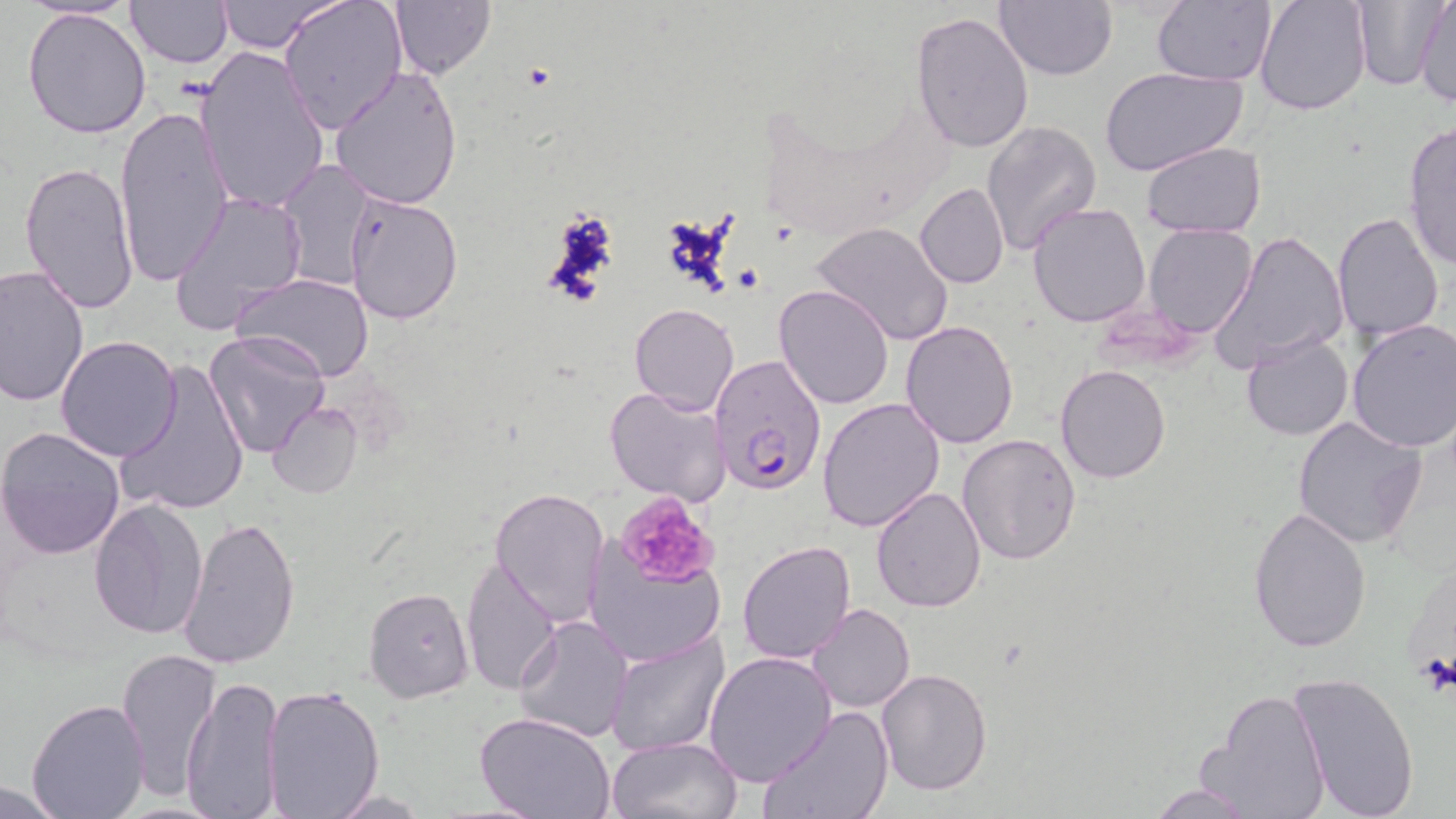
Approximate bounding boxes as named x1/y1/x2/y2 corners in pixels. Uninfected red blood cell locations: (x1=211, y1=0, x2=340, y2=53), (x1=278, y1=0, x2=405, y2=136), (x1=995, y1=0, x2=1116, y2=81), (x1=1151, y1=0, x2=1276, y2=86), (x1=1255, y1=0, x2=1372, y2=116), (x1=1352, y1=0, x2=1443, y2=90), (x1=1414, y1=0, x2=1456, y2=107), (x1=25, y1=1, x2=140, y2=22), (x1=124, y1=1, x2=232, y2=68), (x1=388, y1=1, x2=494, y2=79), (x1=23, y1=7, x2=151, y2=140), (x1=911, y1=12, x2=1036, y2=155), (x1=192, y1=46, x2=331, y2=215), (x1=329, y1=64, x2=464, y2=210), (x1=1099, y1=66, x2=1250, y2=177), (x1=115, y1=104, x2=235, y2=291), (x1=981, y1=120, x2=1102, y2=257), (x1=1401, y1=121, x2=1456, y2=272), (x1=1140, y1=141, x2=1267, y2=239), (x1=19, y1=160, x2=140, y2=316), (x1=279, y1=162, x2=378, y2=292), (x1=915, y1=181, x2=1008, y2=289), (x1=170, y1=190, x2=309, y2=336), (x1=345, y1=191, x2=464, y2=325), (x1=1025, y1=202, x2=1151, y2=328), (x1=1331, y1=212, x2=1445, y2=343), (x1=810, y1=221, x2=954, y2=350), (x1=1143, y1=224, x2=1258, y2=338), (x1=1211, y1=230, x2=1349, y2=371), (x1=0, y1=263, x2=89, y2=404), (x1=235, y1=274, x2=375, y2=383), (x1=774, y1=284, x2=892, y2=410), (x1=630, y1=303, x2=740, y2=416), (x1=1345, y1=318, x2=1456, y2=452), (x1=901, y1=319, x2=1018, y2=449), (x1=204, y1=331, x2=331, y2=459), (x1=1240, y1=333, x2=1354, y2=442), (x1=56, y1=335, x2=182, y2=461), (x1=116, y1=359, x2=250, y2=519), (x1=1054, y1=364, x2=1174, y2=484), (x1=605, y1=385, x2=732, y2=505), (x1=818, y1=396, x2=946, y2=533), (x1=266, y1=402, x2=362, y2=498), (x1=1293, y1=415, x2=1427, y2=550), (x1=0, y1=427, x2=126, y2=559), (x1=957, y1=432, x2=1081, y2=565), (x1=871, y1=485, x2=988, y2=612), (x1=490, y1=487, x2=610, y2=626), (x1=88, y1=496, x2=209, y2=640), (x1=1246, y1=507, x2=1371, y2=654), (x1=181, y1=515, x2=301, y2=671), (x1=583, y1=539, x2=725, y2=668), (x1=736, y1=539, x2=856, y2=665), (x1=460, y1=557, x2=560, y2=696), (x1=363, y1=586, x2=474, y2=703), (x1=807, y1=603, x2=915, y2=713), (x1=513, y1=613, x2=635, y2=742), (x1=604, y1=631, x2=728, y2=755), (x1=115, y1=645, x2=221, y2=802), (x1=704, y1=651, x2=837, y2=785), (x1=876, y1=669, x2=992, y2=795), (x1=1288, y1=672, x2=1421, y2=818), (x1=181, y1=674, x2=283, y2=818), (x1=261, y1=683, x2=383, y2=818), (x1=1197, y1=686, x2=1332, y2=819), (x1=26, y1=698, x2=149, y2=818), (x1=759, y1=705, x2=894, y2=819), (x1=475, y1=713, x2=617, y2=819), (x1=606, y1=736, x2=741, y2=818), (x1=0, y1=780, x2=69, y2=817), (x1=1143, y1=782, x2=1264, y2=818), (x1=324, y1=790, x2=433, y2=817). Plasmodium falciparum-infected red blood cell locations: (x1=710, y1=357, x2=828, y2=495). Platelet locations: (x1=614, y1=493, x2=721, y2=589), (x1=1417, y1=652, x2=1455, y2=699). Slide-level diagnosis: Plasmodium falciparum. Captured at 1000x magnification. May-Grünwald-Giemsa-stained preparation. Thin blood film. One field of a larger specimen. Image is 1456×819 pixels. Optical microscopy.